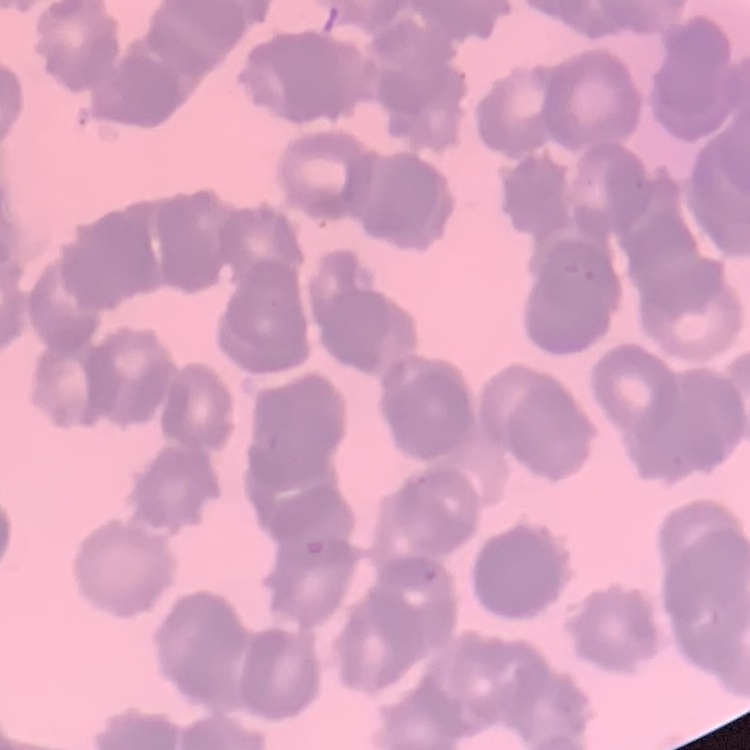 The erythrocytes show rouleaux formation. Field's or Giemsa stain. One tile cut from a larger photomicrograph. Thin blood film.